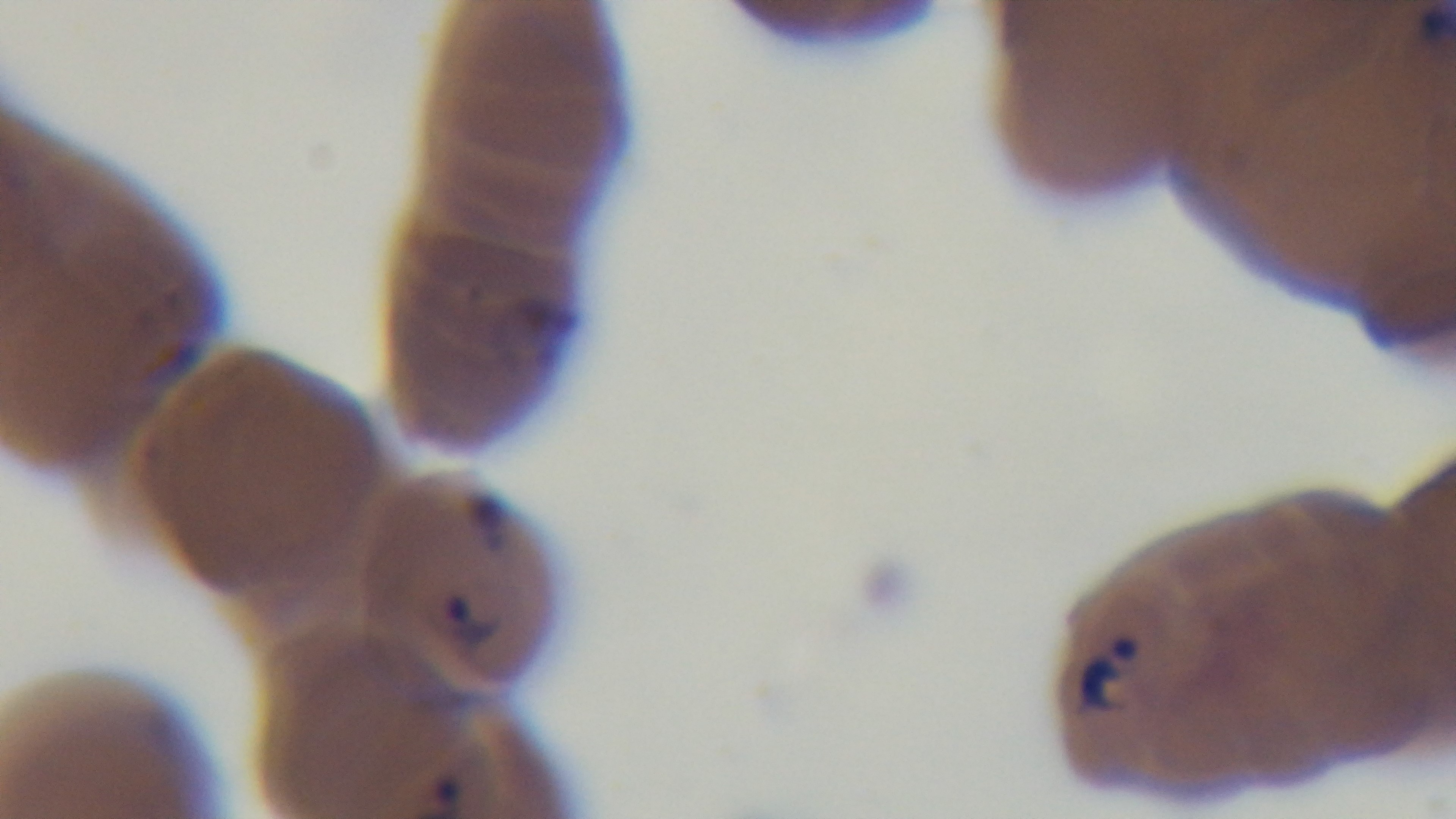
{
  "capture": "mounted 4K digital camera",
  "field_of_view": "single",
  "malaria_status": "infected",
  "stain": "Giemsa",
  "preparation": "thin smear",
  "modality": "light microscopy",
  "objective": "100x oil immersion"
}